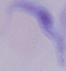
Micrograph. 1000x magnification. A trypanosome is seen.